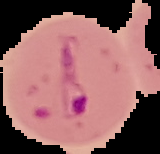 Cell region segmented out of the field of view; the surrounding area is masked to black. Malaria status: parasitized. Image is 160×154 pixels. From a thin blood smear.